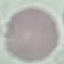
Summary:
  - Malaria status: uninfected
  - Image type: cell patch, automatically extracted from a larger field of view and resized to 64 × 64 pixels
  - Stain: Giemsa
  - Capture: smartphone through the microscope eyepiece
  - Preparation: thin smear